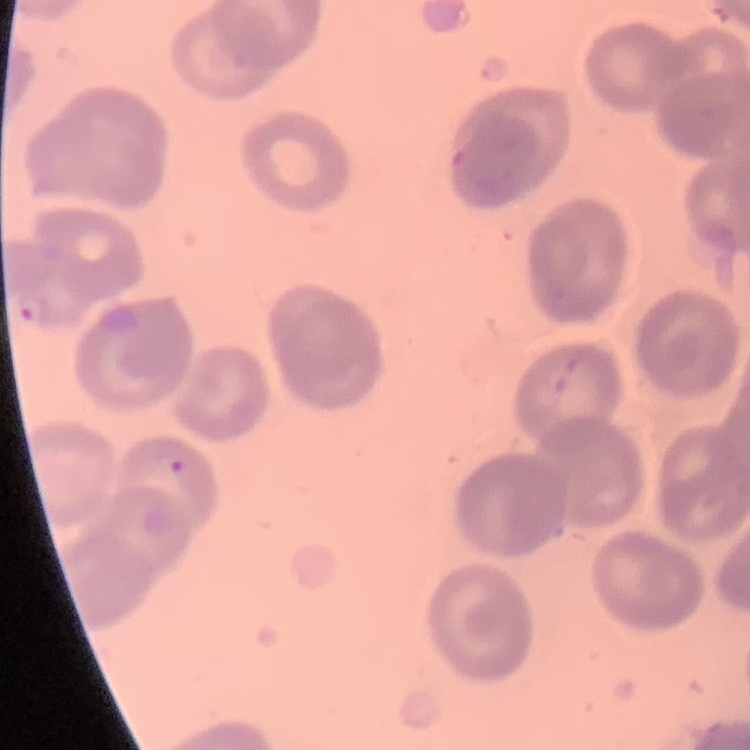

{
  "red_blood_cell_morphology": "no rouleaux formation",
  "preparation": "thin blood smear",
  "stain": "Field's or Giemsa",
  "image_type": "square crop of a larger photomicrograph"
}